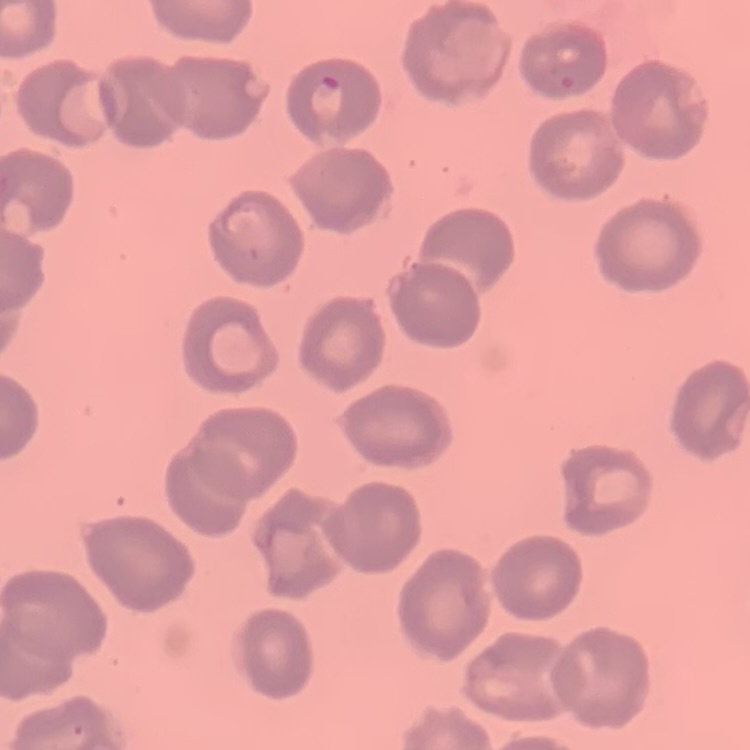

Summary:
  - Erythrocyte morphology: no rouleaux formation
  - Image type: one tile cut from a larger photomicrograph
  - Stain: Field's or Giemsa
  - Preparation: thin blood smear